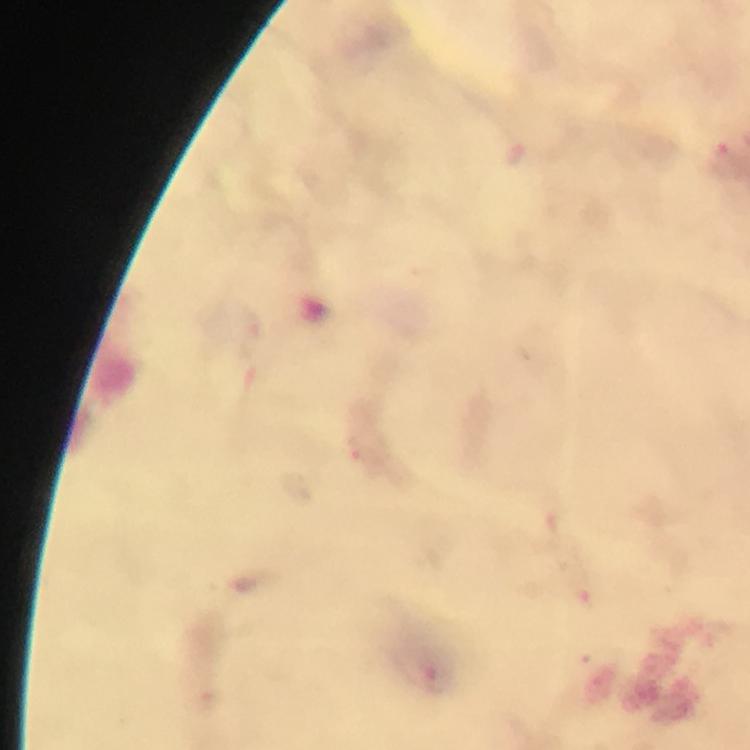

{
  "preparation": "thick blood film",
  "plasmodium_parasite_locations": "approximate object centers, in pixels from the top-left corner: (x=720, y=155), (x=363, y=454), (x=585, y=595), (x=437, y=680)",
  "cropped_from": "a single field of view",
  "context": "from a malaria diagnostic workup",
  "image_size": "750×750 pixels",
  "capture": "smartphone mounted on the microscope",
  "magnification": "100x",
  "stain": "Giemsa",
  "immersion_oil": "applied"
}